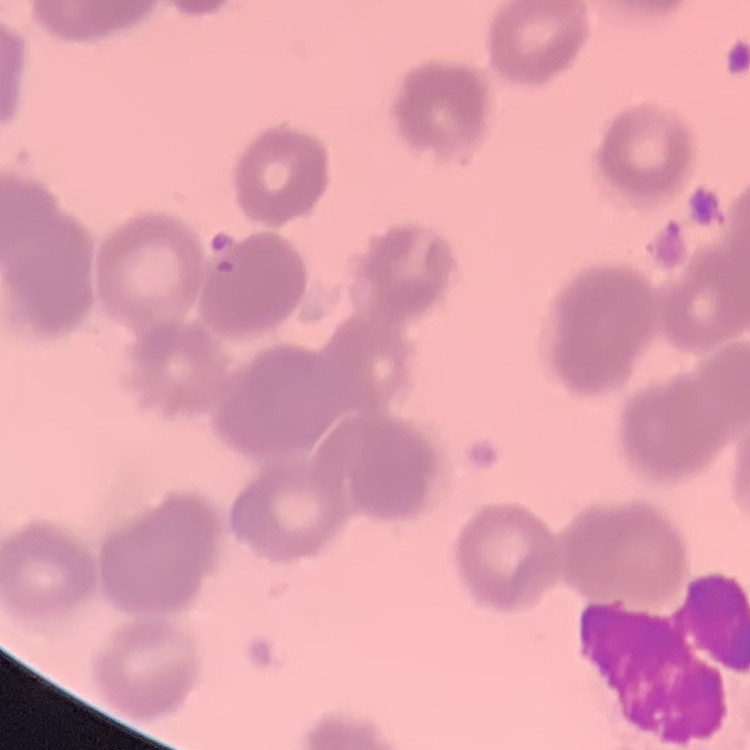

erythrocyte morphology = rouleaux formation
preparation = thin peripheral smear
image type = one tile cut from a larger photomicrograph
stain = Field's or Giemsa